State which cell type is depicted.
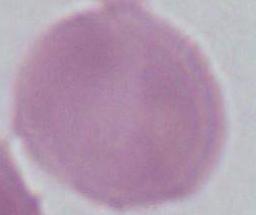
An erythrocyte.

Micrograph. 1000x magnification.